Assess this cell for malaria.
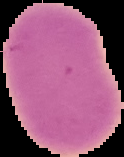
It is uninfected.

Summary:
  - Image size: 124×157 pixels
  - Preparation: thin blood smear
  - Image type: cell region segmented out of the field of view; surrounding area masked to black